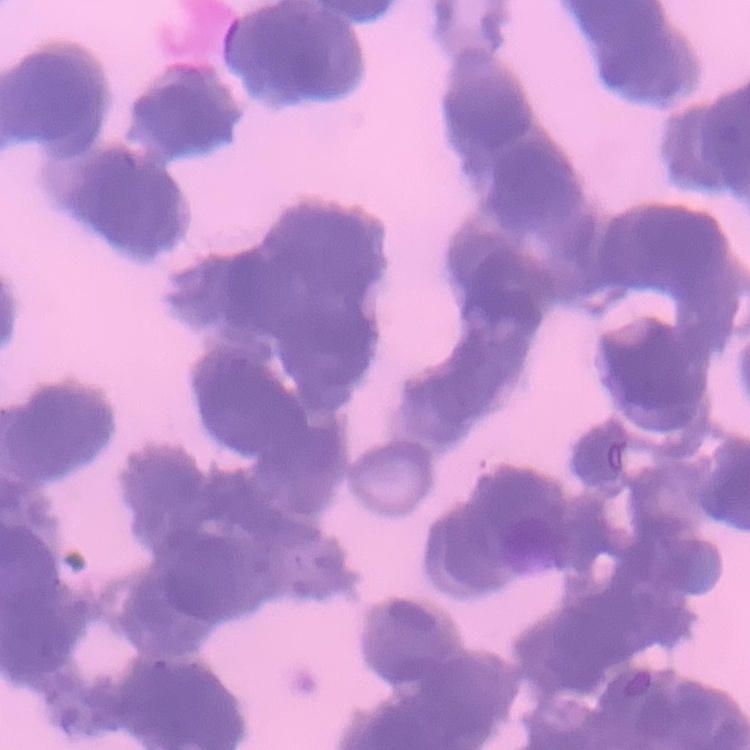
The red blood cells show rouleaux formation. Thin blood film. Stained with either Field's or Giemsa. One tile cut from a larger photomicrograph.